Report the malaria status of this cell.
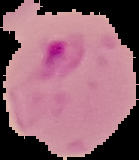
Parasitized.

image size = 139×160 pixels
preparation = thin blood film
image type = segmented cell region with the area outside set to black